State which parasite is depicted.
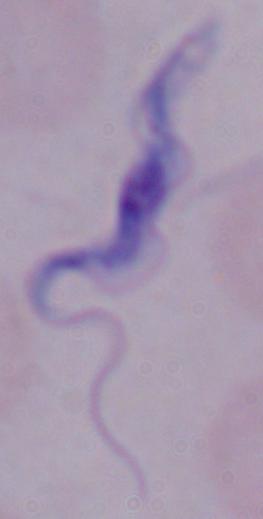
A trypanosome.

Summary:
  - Magnification: 1000x
  - Modality: photomicrograph